Draw a bounding box around every leukocyte (white blood cell).
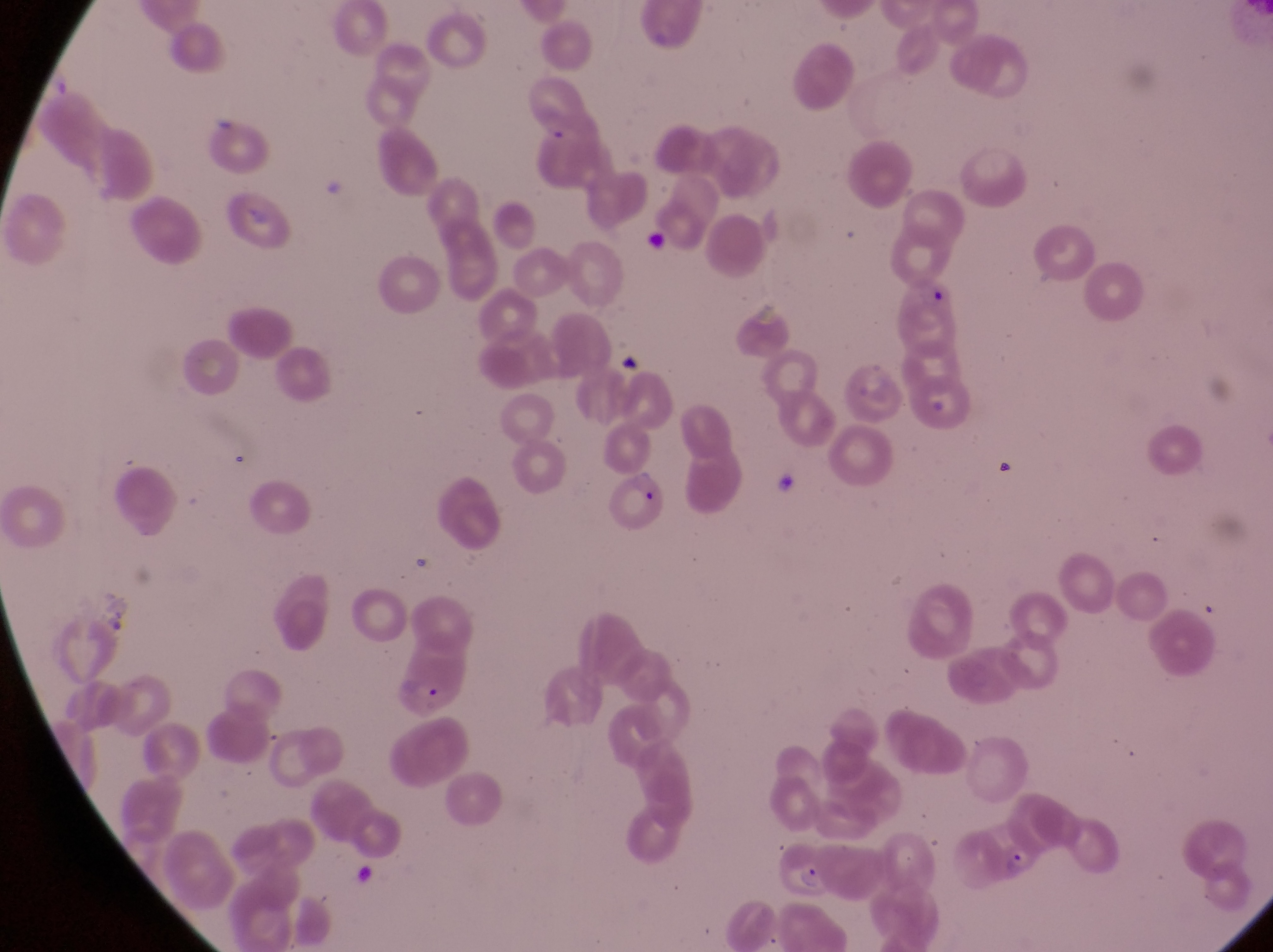
No leukocytes observed.

Approximate bounding boxes as (left, top, right, bottom) in pixels.
Summary:
  - Parasitised red blood cell locations: (609, 465, 672, 535), (385, 664, 473, 724), (976, 817, 1050, 891), (781, 842, 838, 907)
  - Magnification: 1000x
  - Image size: 1273×952 pixels
  - Field of view: single
  - Preparation: thin blood smear
  - Country: Uganda
  - Capture: smartphone photograph through the eyepiece of an Olympus CX-23 microscope